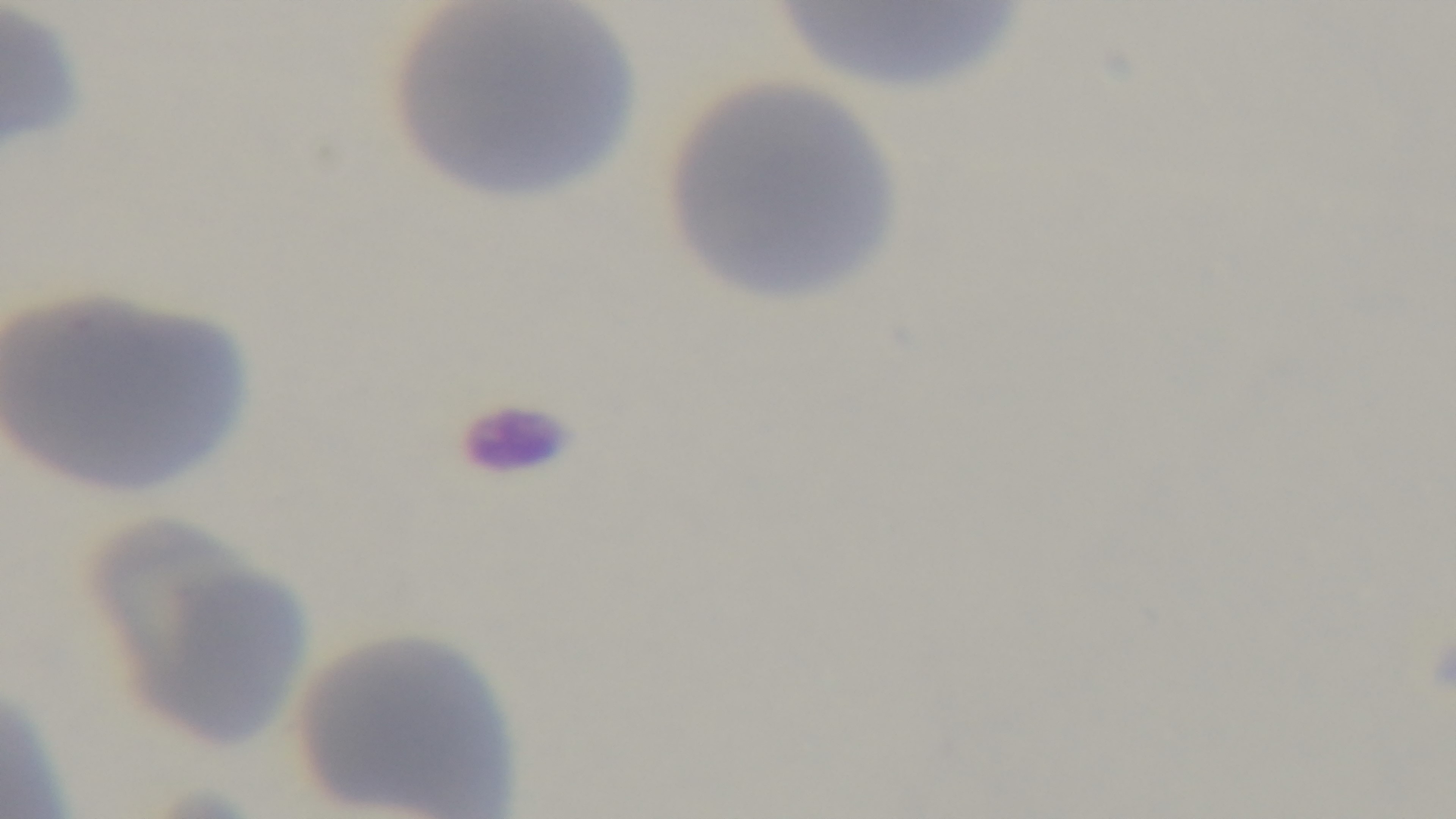
preparation = thin blood film
objective = 100x oil immersion
malaria status = negative
field of view = single
capture = mounted 4K digital camera
modality = light microscopy
stain = Giemsa